State which parasite is depicted.
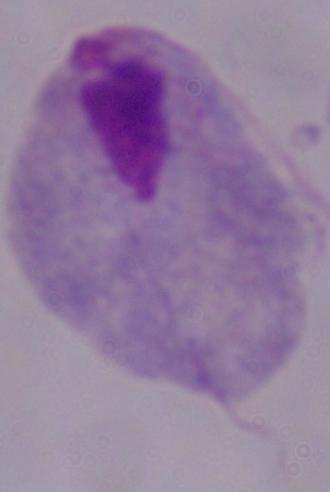

A trichomonad.

magnification: 1000x
modality: photomicrograph